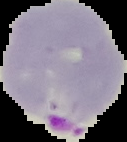 Segmented cell region on a black background. Malaria status: parasitized. From a thin blood smear. Image is 127×142 pixels.